Classify this cell by malaria status.
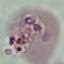
Uninfected.

Cell patch, automatically extracted from a larger field of view and resized to 64 × 64 pixels. Giemsa-stained preparation. Photographed with a smartphone camera at the microscope eyepiece. Thin smear of blood.